Name the parasite shown.
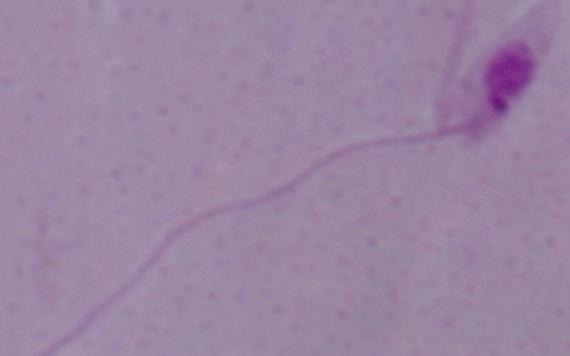

Leishmania.

Summary:
  - Magnification: 1000x
  - Modality: photomicrograph